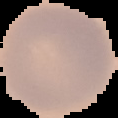
Summary:
  - Preparation: thin blood film
  - Image size: 118×118 pixels
  - Result: no malaria parasites seen
  - Image type: segmented cell region with the area outside set to black